Classify this cell by malaria status.
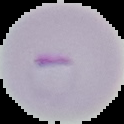
Parasitized.

{
  "image_size": "124×124 pixels",
  "image_type": "segmented cell region with the area outside set to black",
  "preparation": "thin blood film"
}